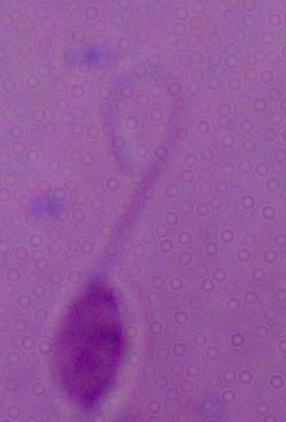 Micrograph. Captured at 1000x magnification. A Leishmania parasite is shown.